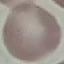

Summary:
  - Result: negative for malaria parasites
  - Capture: smartphone through the microscope eyepiece
  - Preparation: thin blood film
  - Image type: automatically extracted cell patch, resized to 64 × 64 pixels
  - Stain: Giemsa